Name the cell type shown.
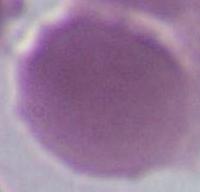

An erythrocyte.

Summary:
  - Magnification: 1000x
  - Modality: micrograph